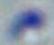

Summary:
  - Modality: photomicrograph
  - Magnification: 1000x
  - Identification: Toxoplasma gondii